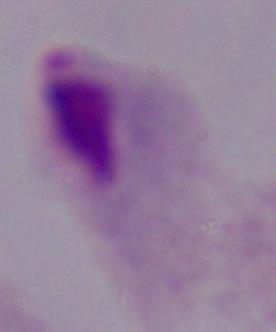

{
  "identification": "trichomonad",
  "magnification": "1000x",
  "modality": "micrograph"
}